Identify the parasite.
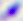
This is Toxoplasma gondii.

modality = micrograph
magnification = 400x